Report the malaria status of this cell.
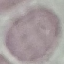

It is uninfected.

capture = smartphone through the microscope eyepiece
stain = Giemsa
preparation = thin blood smear
image type = cell patch, automatically extracted from a larger field of view and resized to 64 × 64 pixels